State which parasite is depicted.
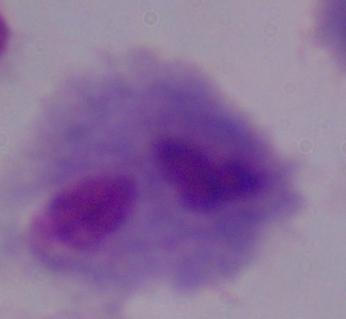
A trichomonad.

modality = micrograph
magnification = 1000x